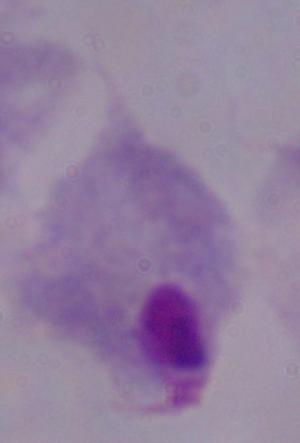
Captured at 1000x magnification. Photomicrograph. A trichomonad is shown.